Comment on the morphology of the erythrocytes.
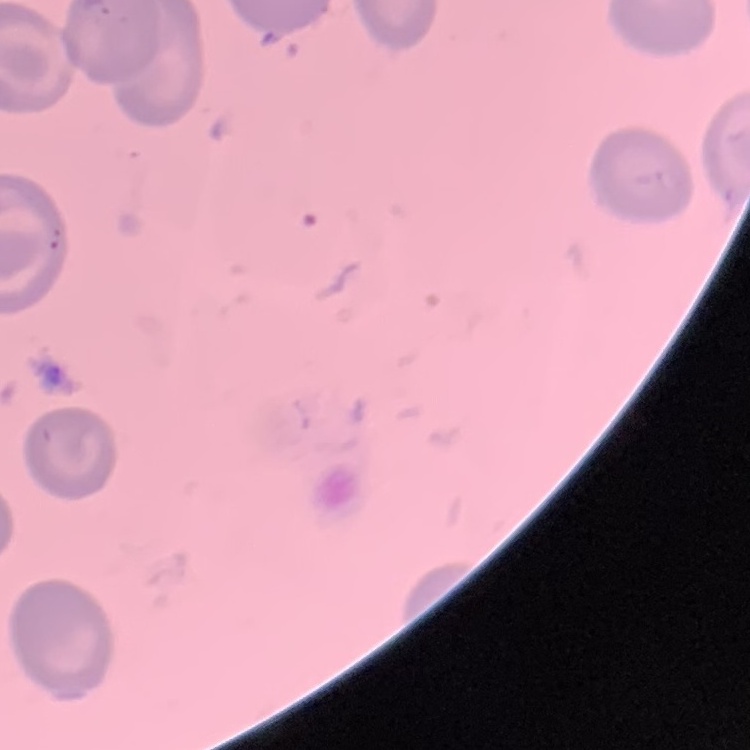

No rouleaux formation.

Summary:
  - Preparation: thin peripheral smear
  - Image type: one tile cut from a larger photomicrograph
  - Stain: Field's or Giemsa